Locate and identify every blood parasite.
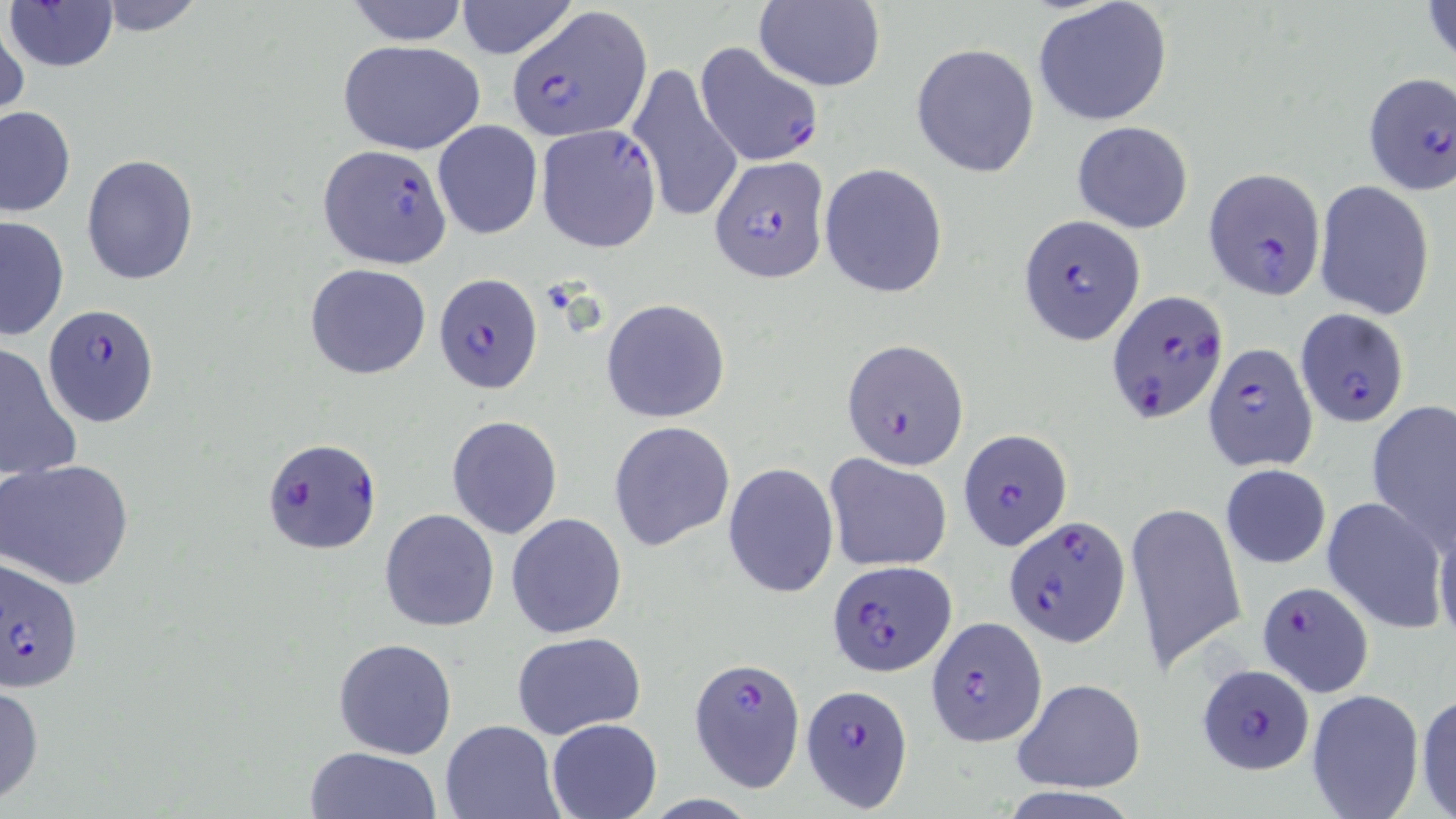

Approximate bounding boxes as [x1, y1, x2, y2] in pixels.
Plasmodium falciparum-infected red blood cells: [506, 7, 650, 139], [693, 40, 826, 169], [1360, 70, 1455, 197], [535, 124, 662, 253], [317, 144, 451, 269], [709, 155, 830, 283], [1203, 166, 1327, 301], [1018, 214, 1147, 345], [432, 272, 544, 394], [1105, 287, 1231, 427], [42, 305, 161, 427], [1296, 307, 1410, 428], [842, 338, 970, 470], [1202, 342, 1315, 473], [958, 429, 1072, 550], [261, 438, 382, 554], [1005, 514, 1130, 646], [3, 554, 84, 690], [824, 557, 957, 675], [1256, 578, 1376, 697], [927, 617, 1048, 745], [692, 656, 803, 794], [1195, 662, 1314, 775], [801, 685, 913, 811].
No Plasmodium ovale, Plasmodium malariae, Plasmodium vivax, Babesia divergens, or Trypanosoma brucei observed.

Uninfected red blood cell locations: [94, 0, 207, 35], [4, 1, 120, 72], [342, 1, 473, 46], [753, 1, 885, 91], [1422, 1, 1455, 70], [453, 2, 578, 58], [1033, 2, 1173, 127], [0, 15, 27, 121], [337, 39, 486, 157], [910, 42, 1040, 178], [627, 61, 744, 229], [0, 105, 76, 216], [432, 119, 543, 240], [1072, 121, 1194, 234], [81, 154, 198, 285], [818, 163, 949, 299], [1314, 180, 1437, 321], [0, 215, 70, 342], [305, 263, 432, 379], [600, 299, 731, 423], [0, 342, 81, 483], [1366, 398, 1456, 550], [446, 415, 563, 539], [609, 420, 735, 550], [823, 454, 950, 572], [1, 459, 134, 589], [723, 461, 838, 598], [1220, 463, 1330, 569], [1322, 496, 1448, 632], [1128, 498, 1246, 674], [379, 508, 500, 632], [506, 513, 627, 639], [1434, 519, 1456, 649], [511, 631, 647, 740], [333, 636, 458, 758], [1012, 677, 1147, 793], [0, 682, 45, 804], [1305, 690, 1424, 818], [1414, 691, 1456, 817], [547, 718, 663, 819], [440, 719, 563, 817], [303, 745, 444, 819]. Slide-level diagnosis: Plasmodium falciparum. May-Grünwald-Giemsa stain. Thin blood smear. Optical microscopy. One field of a larger specimen. 1000x magnification. Image is 1456×819 pixels.